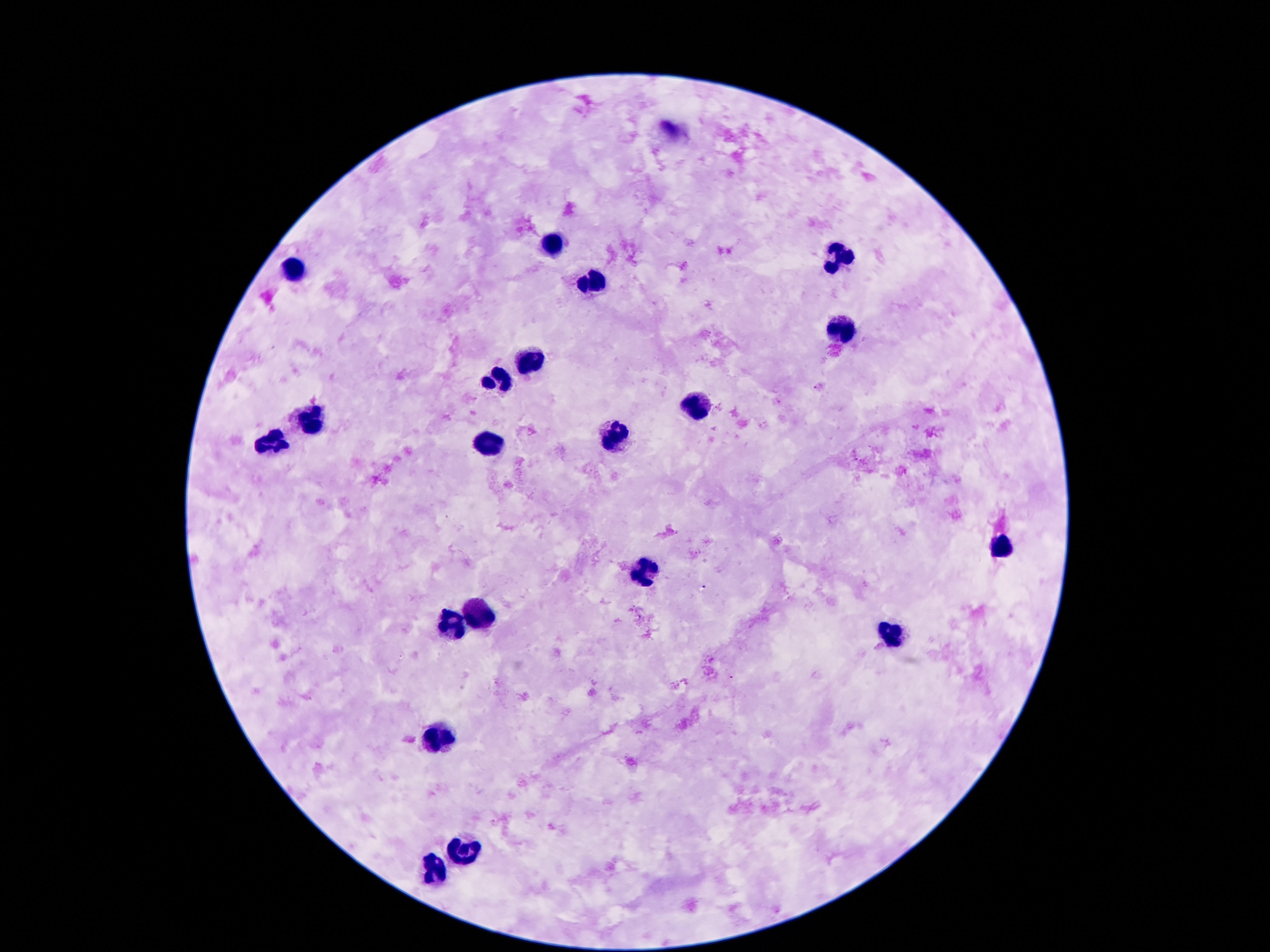 Approximate centers as {x, y} in pixels. Leukocyte locations: {551, 247}, {844, 255}, {289, 269}, {592, 284}, {840, 327}, {528, 358}, {498, 374}, {700, 406}, {315, 423}, {608, 434}, {487, 445}, {266, 447}, {1001, 548}, {647, 573}, {485, 614}, {453, 624}, {891, 636}, {434, 734}, {463, 849}, {436, 870}. Thick blood smear. Photographed through the microscope eyepiece with a smartphone camera. 100x magnification. Giemsa-stained preparation. Image is 1270×952 pixels. Patient malaria status: uninfected. One field from this slide.